Give the position of every Plasmodium parasite.
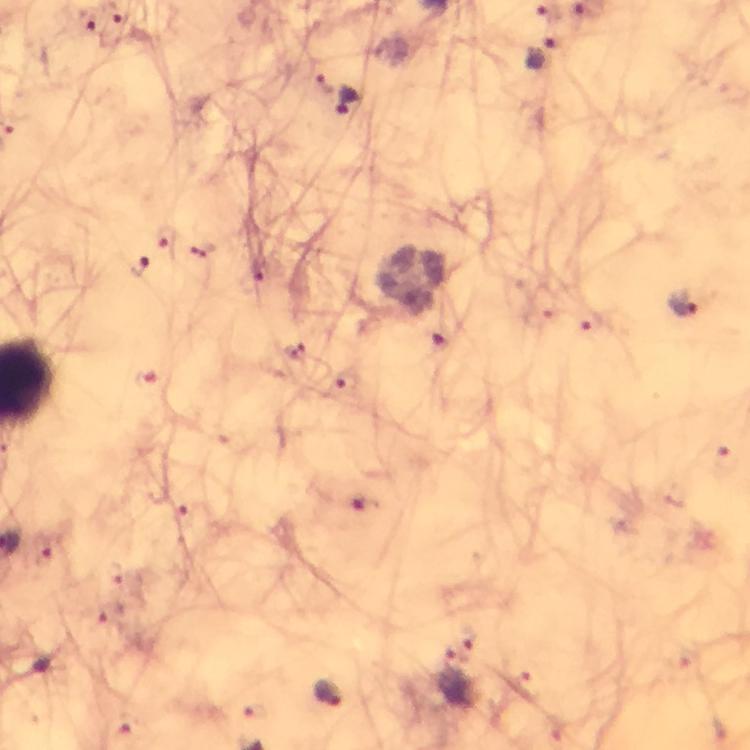

Approximate centers as {x, y} in pixels.
Plasmodium parasites: {112, 17}, {86, 19}, {545, 55}, {324, 85}, {351, 101}, {167, 241}, {135, 267}, {685, 302}, {441, 338}, {146, 379}, {346, 382}, {186, 529}, {469, 638}, {448, 658}, {329, 694}.

{
  "preparation": "thick blood film",
  "capture": "smartphone mounted on the microscope",
  "stain": "Giemsa",
  "context": "from a diagnostic examination for malaria",
  "magnification": "100x",
  "immersion_oil": "used",
  "cropped_from": "one field of view",
  "image_size": "750×750 pixels"
}